Report the malaria status of this cell.
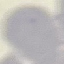
It is uninfected.

Thin blood film. Giemsa stain. Automatically extracted cell patch, resized to 64 × 64 pixels. Acquired by smartphone through the microscope eyepiece.